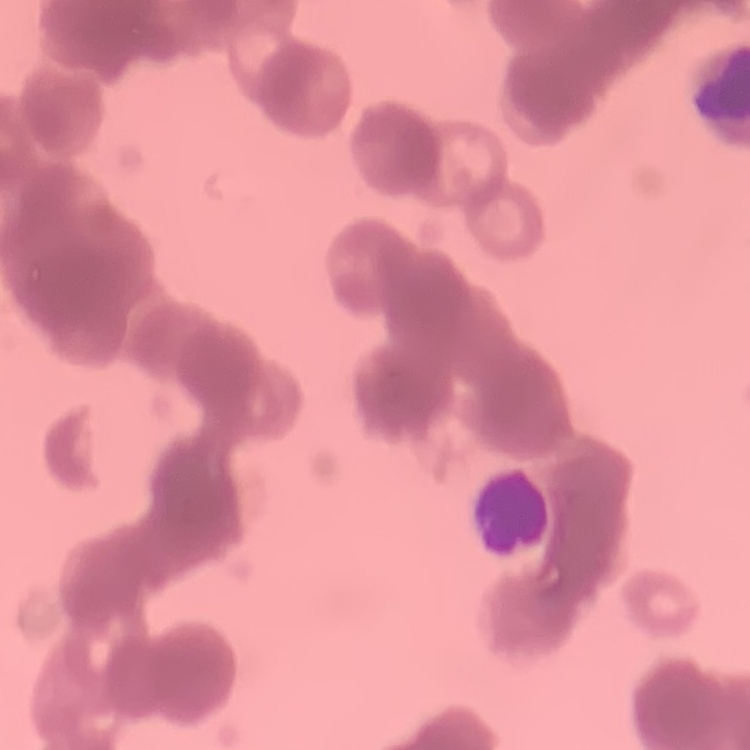
The erythrocytes show rouleaux formation. One tile cut from a larger photomicrograph. Field's or Giemsa stain. Thin blood film.